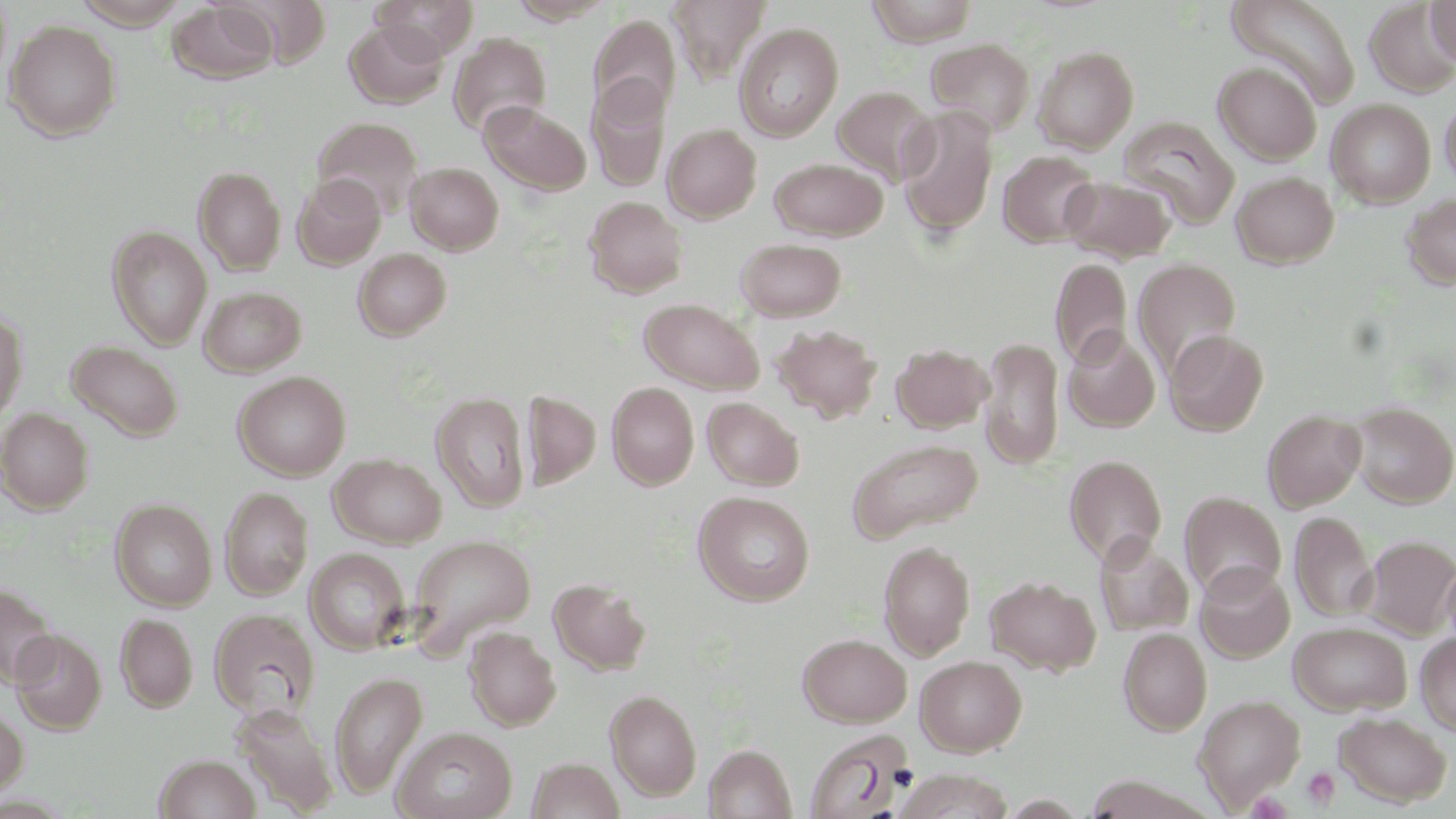
Summary:
  - Coordinate format: approximate bounding boxes as named x1/y1/x2/y2 corners in pixels
  - Uninfected red blood cell locations: (x1=0, y1=0, x2=12, y2=87), (x1=73, y1=0, x2=190, y2=29), (x1=229, y1=0, x2=331, y2=68), (x1=373, y1=0, x2=479, y2=60), (x1=507, y1=0, x2=616, y2=24), (x1=668, y1=0, x2=771, y2=83), (x1=866, y1=0, x2=980, y2=46), (x1=1424, y1=0, x2=1456, y2=66), (x1=1226, y1=1, x2=1360, y2=107), (x1=167, y1=2, x2=278, y2=84), (x1=1364, y1=3, x2=1455, y2=97), (x1=588, y1=14, x2=681, y2=120), (x1=4, y1=19, x2=121, y2=141), (x1=345, y1=19, x2=449, y2=108), (x1=734, y1=23, x2=844, y2=141), (x1=448, y1=32, x2=552, y2=138), (x1=925, y1=37, x2=1036, y2=137), (x1=1033, y1=46, x2=1139, y2=153), (x1=1213, y1=61, x2=1322, y2=165), (x1=587, y1=77, x2=671, y2=192), (x1=832, y1=85, x2=937, y2=184), (x1=1440, y1=96, x2=1456, y2=189), (x1=1326, y1=98, x2=1436, y2=208), (x1=480, y1=101, x2=591, y2=195), (x1=895, y1=106, x2=999, y2=238), (x1=312, y1=116, x2=424, y2=219), (x1=1117, y1=116, x2=1239, y2=228), (x1=663, y1=123, x2=762, y2=222), (x1=998, y1=150, x2=1101, y2=247), (x1=769, y1=158, x2=888, y2=240), (x1=405, y1=162, x2=503, y2=255), (x1=194, y1=166, x2=286, y2=275), (x1=1231, y1=171, x2=1339, y2=268), (x1=292, y1=173, x2=386, y2=268), (x1=1060, y1=174, x2=1177, y2=263), (x1=1401, y1=192, x2=1456, y2=290), (x1=584, y1=196, x2=687, y2=297), (x1=107, y1=225, x2=212, y2=350), (x1=736, y1=238, x2=846, y2=321), (x1=353, y1=248, x2=451, y2=340), (x1=1050, y1=257, x2=1132, y2=368), (x1=1133, y1=258, x2=1241, y2=376), (x1=199, y1=285, x2=306, y2=376), (x1=639, y1=298, x2=764, y2=394), (x1=0, y1=312, x2=27, y2=423), (x1=772, y1=324, x2=883, y2=423), (x1=1062, y1=328, x2=1160, y2=433), (x1=1165, y1=329, x2=1268, y2=436), (x1=979, y1=337, x2=1065, y2=469), (x1=65, y1=340, x2=184, y2=442), (x1=892, y1=343, x2=992, y2=432), (x1=233, y1=371, x2=351, y2=480), (x1=607, y1=382, x2=699, y2=490), (x1=522, y1=391, x2=601, y2=488), (x1=431, y1=392, x2=530, y2=512), (x1=702, y1=397, x2=804, y2=491), (x1=1348, y1=401, x2=1456, y2=508), (x1=0, y1=408, x2=94, y2=514), (x1=1262, y1=409, x2=1366, y2=512), (x1=848, y1=438, x2=984, y2=542), (x1=330, y1=454, x2=447, y2=548), (x1=1064, y1=454, x2=1167, y2=566), (x1=220, y1=486, x2=313, y2=600), (x1=693, y1=490, x2=814, y2=606), (x1=1179, y1=491, x2=1286, y2=600), (x1=111, y1=499, x2=216, y2=610), (x1=1290, y1=511, x2=1376, y2=622), (x1=409, y1=534, x2=536, y2=652), (x1=1094, y1=535, x2=1194, y2=636), (x1=1360, y1=535, x2=1456, y2=639), (x1=878, y1=540, x2=976, y2=660), (x1=305, y1=548, x2=411, y2=654), (x1=1441, y1=554, x2=1456, y2=655), (x1=1194, y1=562, x2=1295, y2=663), (x1=985, y1=576, x2=1101, y2=675), (x1=548, y1=577, x2=651, y2=675), (x1=0, y1=584, x2=59, y2=688), (x1=209, y1=608, x2=320, y2=720), (x1=116, y1=613, x2=197, y2=712), (x1=1288, y1=620, x2=1412, y2=716), (x1=464, y1=627, x2=561, y2=730), (x1=1118, y1=628, x2=1211, y2=735), (x1=11, y1=629, x2=106, y2=734), (x1=1415, y1=632, x2=1456, y2=736), (x1=797, y1=633, x2=911, y2=727), (x1=915, y1=655, x2=1027, y2=756), (x1=330, y1=671, x2=428, y2=797), (x1=605, y1=689, x2=702, y2=801), (x1=1193, y1=694, x2=1306, y2=809), (x1=232, y1=701, x2=337, y2=815), (x1=0, y1=704, x2=28, y2=798), (x1=1334, y1=711, x2=1452, y2=807), (x1=392, y1=726, x2=518, y2=819), (x1=805, y1=731, x2=914, y2=817), (x1=704, y1=744, x2=797, y2=819), (x1=154, y1=753, x2=261, y2=819), (x1=527, y1=757, x2=624, y2=819), (x1=893, y1=770, x2=1012, y2=818)
  - Platelet locations: (x1=1303, y1=767, x2=1341, y2=808)
  - Slide-level diagnosis: negative for blood parasites
  - Preparation: thin blood film
  - Stain: May-Grünwald-Giemsa
  - Field of view: one of a larger specimen
  - Image size: 1456×819 pixels
  - Modality: light microscopy
  - Magnification: 1000x